Describe the morphology of the red blood cells.
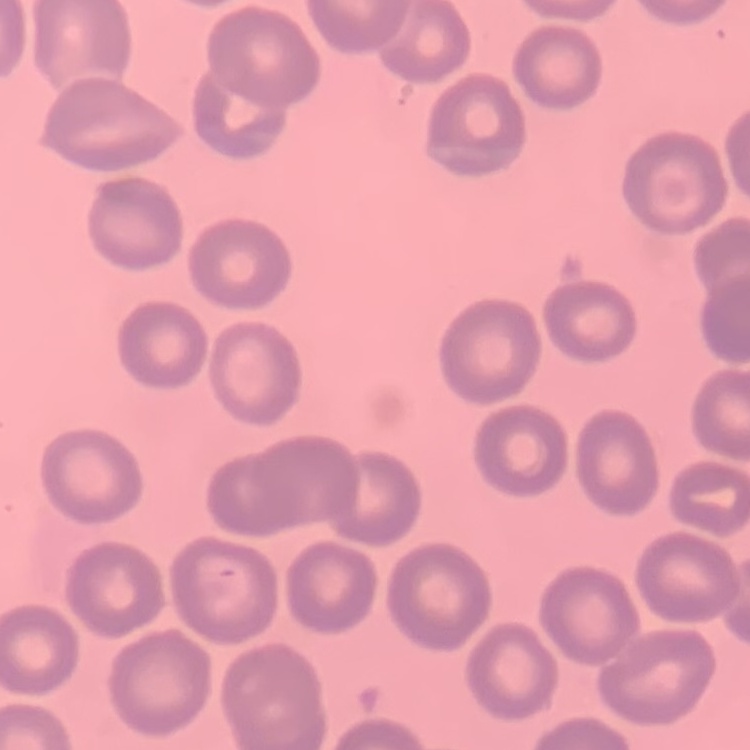
No rouleaux formation.

Square crop of a larger photomicrograph. Field's or Giemsa stain. Thin blood film.